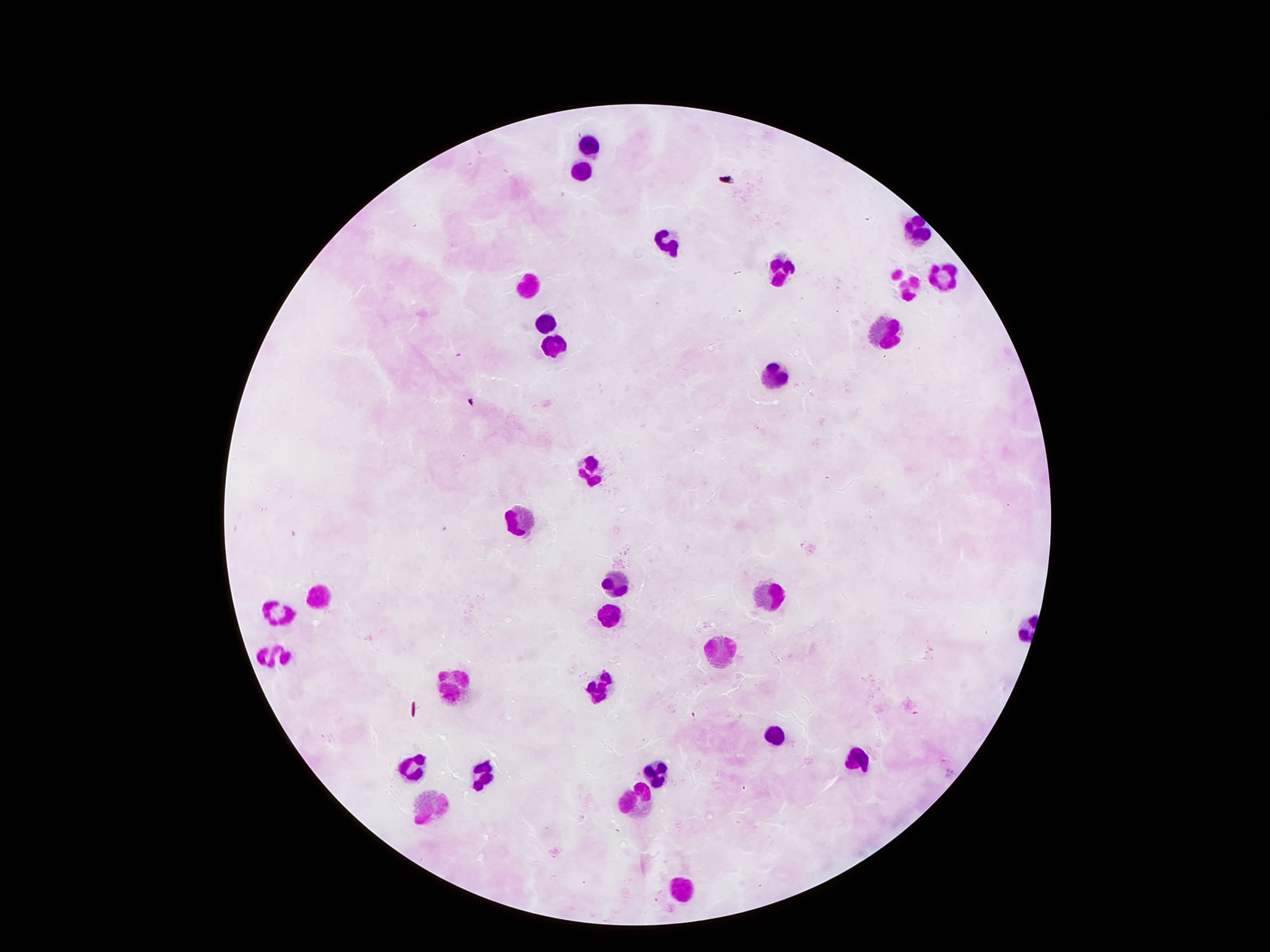
patient_malaria_status: not infected
field_of_view: single
stain: Giemsa
magnification: 100x
capture: smartphone camera through the microscope eyepiece
leukocyte_locations: 'approximate centers as (x, y) in pixels: (593, 143), (581, 172), (917, 226), (672, 243), (779, 269), (944, 275), (529, 285), (903, 289), (541, 322), (879, 336), (554, 345), (773, 374), (594, 466), (512, 517), (619, 584), (314, 596), (763, 596), (281, 609), (602, 618), (279, 652), (718, 652), (460, 688), (603, 694), (772, 737), (861, 760), (410, 770), (658, 771), (485, 775), (632, 803), (430, 808), (682, 884)'
image_size: 1270×952 pixels
preparation: thick blood smear